Identify the cell.
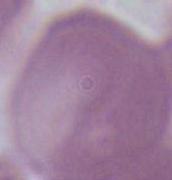

An erythrocyte.

modality: photomicrograph
magnification: 1000x